Comment on the morphology of the red blood cells.
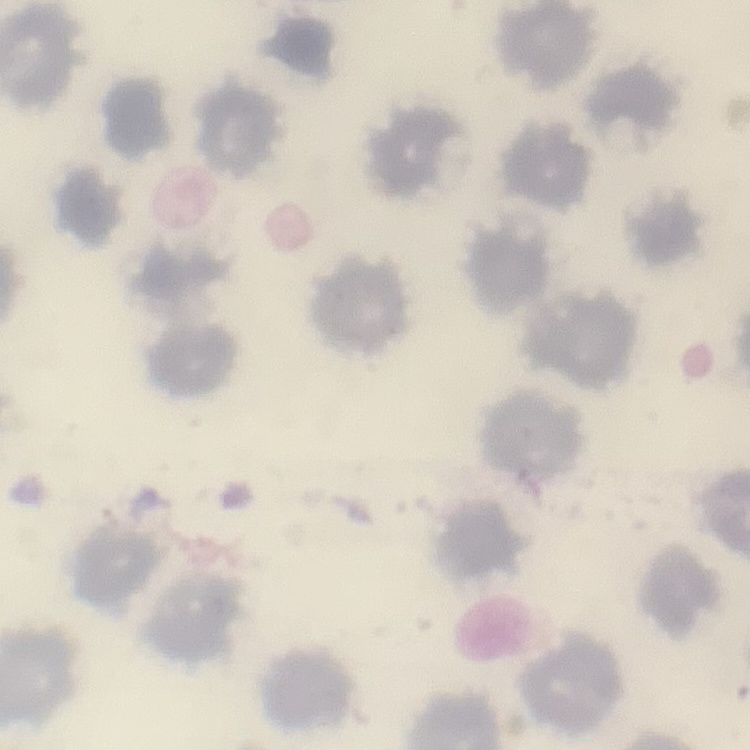
No rouleaux formation.

stain = Field's or Giemsa
image type = square crop of a larger photomicrograph
preparation = thin peripheral smear